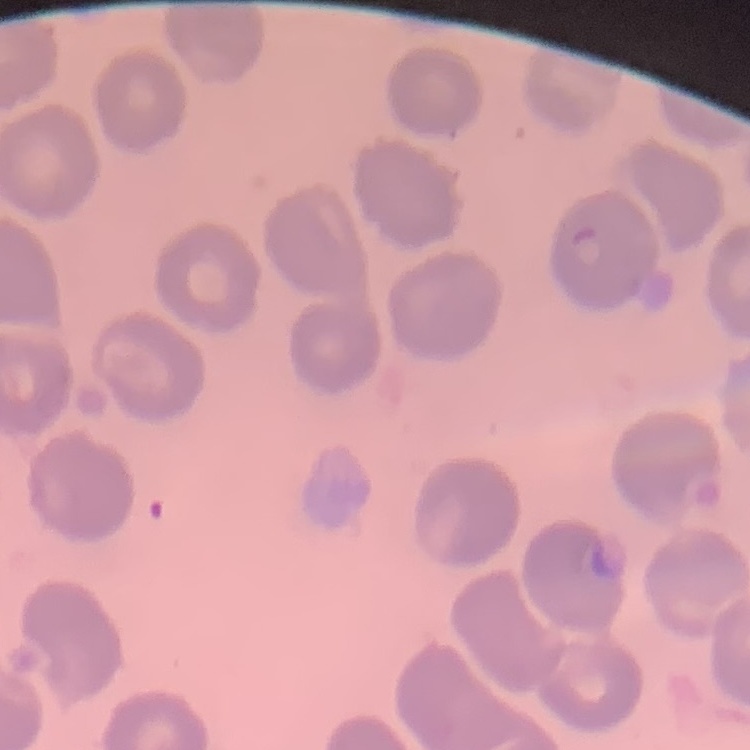
Summary:
  - Erythrocyte morphology: no rouleaux formation
  - Preparation: thin peripheral smear
  - Image type: one tile cut from a larger photomicrograph
  - Stain: Field's or Giemsa